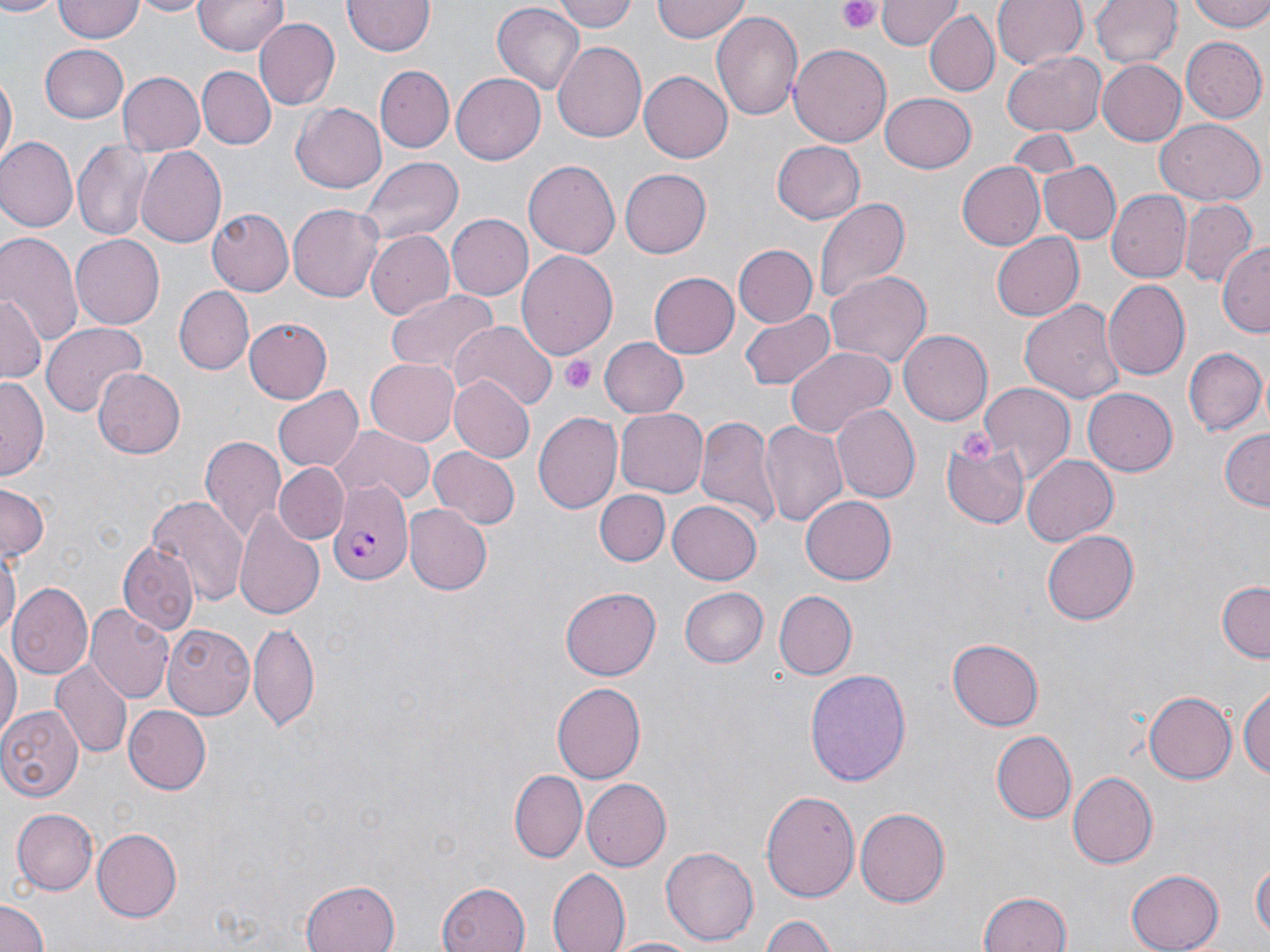

slide-level diagnosis = Plasmodium falciparum
platelet locations = approximate bounding boxes as [x1, y1, x2, y2] in pixels: [839, 0, 883, 36], [560, 355, 594, 394], [956, 429, 994, 465]
magnification = 1000x
stain = May-Grünwald-Giemsa
modality = optical microscopy
Plasmodium falciparum-infected red blood cell locations = approximate bounding boxes as [x1, y1, x2, y2] in pixels: [328, 479, 413, 586]
uninfected red blood cell locations = approximate bounding boxes as [x1, y1, x2, y2] in pixels: [54, 0, 145, 42], [133, 0, 208, 17], [194, 0, 286, 57], [552, 0, 636, 32], [654, 0, 750, 42], [877, 0, 957, 49], [993, 0, 1087, 71], [1090, 0, 1179, 70], [1185, 0, 1270, 31], [0, 1, 57, 19], [343, 1, 434, 57], [491, 4, 585, 97], [709, 8, 803, 121], [924, 10, 999, 97], [253, 17, 339, 110], [1181, 38, 1266, 122], [552, 42, 647, 145], [40, 44, 129, 123], [790, 45, 891, 147], [1002, 51, 1107, 138], [1098, 58, 1189, 144], [376, 66, 454, 151], [197, 67, 272, 147], [639, 71, 733, 162], [118, 72, 204, 155], [452, 73, 546, 164], [1, 74, 16, 170], [880, 92, 977, 173], [292, 101, 387, 193], [1155, 118, 1266, 206], [1005, 127, 1081, 188], [72, 138, 152, 240], [0, 139, 77, 233], [770, 140, 866, 226], [136, 147, 228, 248], [355, 155, 463, 246], [523, 160, 620, 261], [1042, 162, 1119, 244], [956, 163, 1044, 249], [617, 167, 710, 260], [1106, 188, 1191, 283], [813, 196, 909, 308], [1180, 200, 1256, 288], [287, 203, 386, 302], [206, 209, 291, 297], [446, 215, 532, 298], [0, 230, 81, 347], [991, 230, 1084, 322], [365, 231, 455, 321], [70, 233, 164, 327], [733, 244, 819, 327], [1220, 245, 1270, 336], [516, 251, 618, 360], [825, 269, 932, 369], [648, 271, 740, 359], [1104, 280, 1191, 380], [173, 285, 254, 375], [388, 288, 499, 381], [0, 291, 44, 382], [1019, 296, 1125, 403], [737, 307, 837, 392], [245, 319, 334, 404], [40, 321, 146, 418], [450, 321, 554, 412], [899, 329, 992, 426], [599, 337, 689, 418], [785, 347, 894, 437], [1185, 347, 1267, 434], [365, 355, 463, 445], [92, 368, 185, 459], [451, 373, 535, 461], [0, 374, 49, 478], [979, 382, 1073, 483], [275, 388, 362, 472], [1084, 388, 1178, 476], [833, 405, 919, 505], [613, 408, 708, 498], [533, 411, 622, 514], [696, 414, 779, 528], [758, 419, 848, 531], [331, 424, 435, 506], [1218, 429, 1269, 512], [199, 433, 286, 544], [942, 435, 1028, 530], [429, 446, 519, 529], [1023, 453, 1118, 544], [272, 463, 349, 545], [0, 484, 48, 562], [596, 489, 669, 567], [801, 492, 897, 583], [147, 495, 246, 611], [668, 499, 762, 585], [404, 504, 492, 595], [234, 507, 324, 622], [1042, 531, 1137, 625], [117, 541, 197, 634], [0, 544, 19, 649], [8, 580, 94, 679], [1215, 580, 1270, 663], [560, 585, 661, 680], [680, 585, 767, 668], [774, 591, 856, 679], [86, 603, 173, 701], [249, 621, 319, 733], [164, 625, 255, 719], [0, 638, 19, 747], [947, 638, 1043, 731], [50, 661, 132, 760], [804, 666, 911, 786], [1240, 679, 1270, 784], [552, 682, 645, 783], [1145, 689, 1239, 783], [122, 704, 210, 793], [1, 705, 82, 801], [991, 731, 1076, 823], [509, 770, 586, 864], [1067, 770, 1158, 868], [581, 778, 670, 871], [762, 787, 860, 905], [11, 806, 98, 895], [855, 808, 949, 907], [90, 827, 181, 921], [660, 844, 759, 945], [1251, 859, 1269, 946], [549, 868, 631, 952], [1124, 868, 1224, 951], [301, 879, 402, 952], [436, 882, 529, 952], [976, 891, 1073, 952], [0, 899, 49, 952], [759, 914, 840, 952], [608, 936, 705, 952]
preparation = thin blood smear
image size = 1270×952 pixels
field of view = single